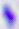

{
  "magnification": "400x",
  "modality": "photomicrograph",
  "identification": "Toxoplasma gondii"
}